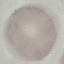

malaria_status: uninfected
image_type: cell patch, automatically extracted from a larger field of view and resized to 64 × 64 pixels
preparation: thin blood film
capture: smartphone camera at the microscope eyepiece
stain: Giemsa